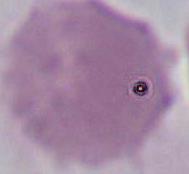
Summary:
  - Identification: red blood cell
  - Magnification: 1000x
  - Modality: photomicrograph